Classify this cell by malaria status.
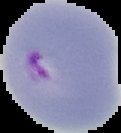

Parasitized.

Image is 121×133 pixels. Cell region segmented out of the field of view; the surrounding area is masked to black. From a thin blood smear.